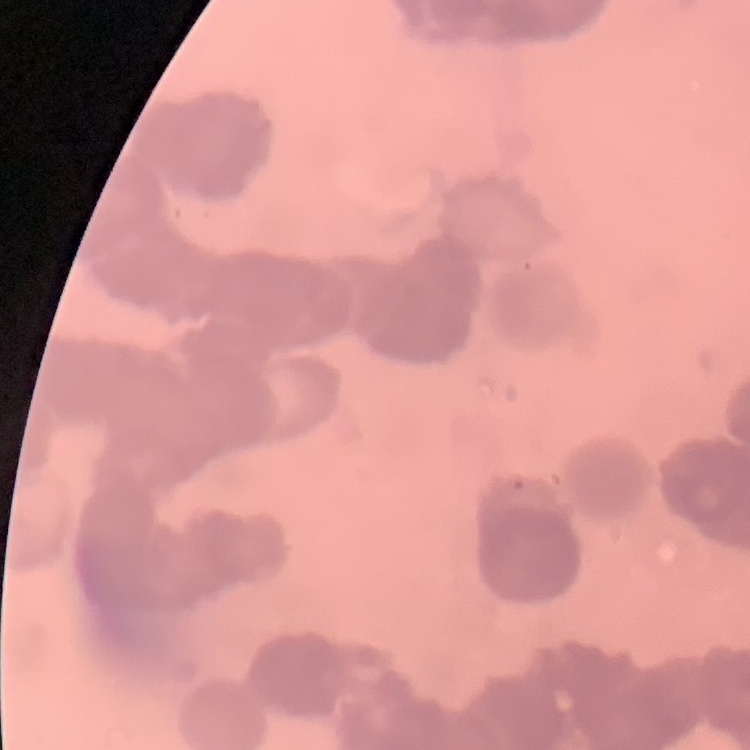

Summary:
  - Erythrocyte morphology: rouleaux formation
  - Stain: Field's or Giemsa
  - Preparation: thin peripheral smear
  - Image type: one tile cut from a larger photomicrograph